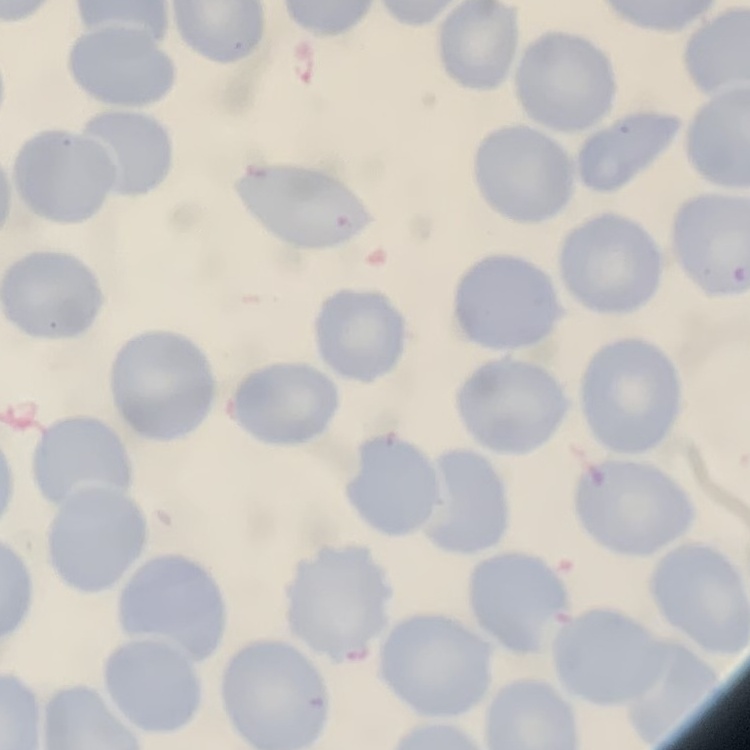
The red blood cells exhibit no rouleaux formation. Field's or Giemsa stain. Square crop of a larger photomicrograph. Thin blood smear.